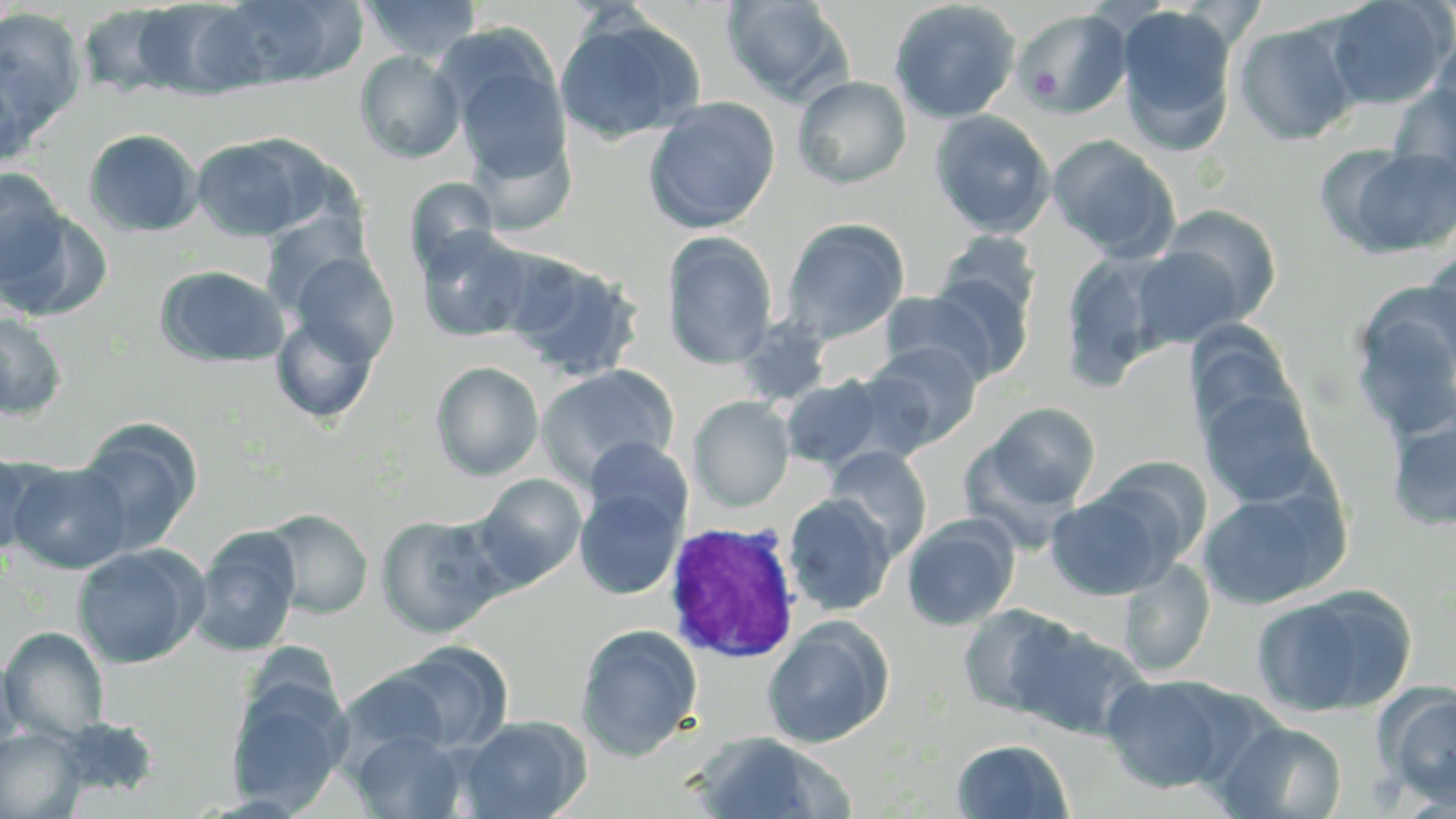 Approximate bounding boxes as named x1/y1/x2/y2 corners in pixels. White blood cell locations: (x1=662, y1=520, x2=801, y2=664). Platelet locations: (x1=1027, y1=66, x2=1062, y2=100). Uninfected red blood cell locations: (x1=217, y1=0, x2=364, y2=88), (x1=362, y1=0, x2=482, y2=62), (x1=1322, y1=0, x2=1454, y2=110), (x1=131, y1=1, x2=259, y2=100), (x1=721, y1=1, x2=854, y2=106), (x1=889, y1=1, x2=1021, y2=124), (x1=77, y1=4, x2=186, y2=98), (x1=1115, y1=5, x2=1237, y2=153), (x1=1013, y1=8, x2=1133, y2=120), (x1=0, y1=9, x2=86, y2=138), (x1=554, y1=13, x2=705, y2=144), (x1=1232, y1=19, x2=1360, y2=145), (x1=1430, y1=22, x2=1456, y2=136), (x1=448, y1=46, x2=573, y2=185), (x1=354, y1=50, x2=466, y2=164), (x1=0, y1=53, x2=44, y2=171), (x1=793, y1=75, x2=912, y2=189), (x1=1388, y1=82, x2=1456, y2=194), (x1=643, y1=97, x2=781, y2=235), (x1=931, y1=110, x2=1055, y2=238), (x1=83, y1=128, x2=203, y2=237), (x1=467, y1=132, x2=575, y2=237), (x1=1047, y1=135, x2=1181, y2=262), (x1=192, y1=136, x2=317, y2=242), (x1=1327, y1=144, x2=1456, y2=260), (x1=0, y1=168, x2=69, y2=287), (x1=403, y1=177, x2=501, y2=281), (x1=1155, y1=204, x2=1281, y2=328), (x1=1, y1=206, x2=112, y2=323), (x1=781, y1=218, x2=910, y2=344), (x1=415, y1=225, x2=538, y2=342), (x1=662, y1=231, x2=778, y2=369), (x1=937, y1=231, x2=1041, y2=322), (x1=1423, y1=244, x2=1456, y2=368), (x1=1129, y1=245, x2=1245, y2=347), (x1=286, y1=250, x2=399, y2=365), (x1=1059, y1=250, x2=1177, y2=389), (x1=499, y1=251, x2=645, y2=382), (x1=154, y1=265, x2=289, y2=368), (x1=921, y1=270, x2=1034, y2=383), (x1=879, y1=290, x2=999, y2=383), (x1=1350, y1=290, x2=1456, y2=444), (x1=270, y1=312, x2=380, y2=424), (x1=0, y1=314, x2=68, y2=421), (x1=1184, y1=324, x2=1301, y2=445), (x1=864, y1=341, x2=983, y2=452), (x1=430, y1=361, x2=544, y2=481), (x1=536, y1=364, x2=679, y2=487), (x1=781, y1=374, x2=887, y2=469), (x1=1196, y1=384, x2=1324, y2=511), (x1=688, y1=396, x2=795, y2=511), (x1=977, y1=403, x2=1102, y2=514), (x1=1386, y1=416, x2=1456, y2=531), (x1=74, y1=418, x2=203, y2=553), (x1=583, y1=437, x2=693, y2=536), (x1=825, y1=446, x2=932, y2=560), (x1=0, y1=450, x2=44, y2=559), (x1=1090, y1=456, x2=1213, y2=569), (x1=6, y1=460, x2=134, y2=574), (x1=473, y1=473, x2=588, y2=590), (x1=1195, y1=484, x2=1347, y2=609), (x1=574, y1=486, x2=685, y2=600), (x1=1046, y1=490, x2=1171, y2=600), (x1=784, y1=493, x2=896, y2=616), (x1=260, y1=508, x2=373, y2=619), (x1=375, y1=514, x2=506, y2=638), (x1=901, y1=514, x2=1019, y2=630), (x1=190, y1=527, x2=301, y2=656), (x1=72, y1=543, x2=208, y2=669), (x1=1119, y1=557, x2=1214, y2=677), (x1=1113, y1=559, x2=1224, y2=797), (x1=1250, y1=586, x2=1415, y2=719), (x1=958, y1=602, x2=1082, y2=719), (x1=762, y1=617, x2=894, y2=748), (x1=575, y1=623, x2=703, y2=761), (x1=1011, y1=623, x2=1151, y2=742), (x1=1, y1=626, x2=110, y2=740), (x1=387, y1=641, x2=513, y2=753), (x1=0, y1=653, x2=26, y2=763), (x1=337, y1=669, x2=453, y2=763), (x1=1101, y1=673, x2=1244, y2=794), (x1=224, y1=682, x2=349, y2=810), (x1=1378, y1=682, x2=1456, y2=805), (x1=458, y1=714, x2=591, y2=819), (x1=1213, y1=718, x2=1348, y2=818), (x1=0, y1=727, x2=86, y2=818), (x1=351, y1=730, x2=467, y2=818), (x1=687, y1=731, x2=853, y2=818), (x1=951, y1=738, x2=1073, y2=818). Slide-level diagnosis: Plasmodium ovale. One field of a larger specimen. Image is 1456×819 pixels. Light microscopy. Thin blood film. 1000x magnification. May-Grünwald-Giemsa-stained preparation.